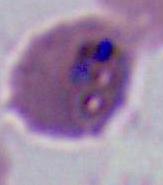
Captured at either 400x or 1000x magnification. Photomicrograph. A Plasmodium parasite is seen.